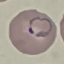

{
  "malaria_status": "parasitized",
  "image_type": "automatically extracted cell patch, resized to 64 × 64 pixels",
  "preparation": "thin blood film",
  "stain": "Giemsa",
  "capture": "smartphone through the microscope eyepiece"
}